Point out Plasmodium parasites and leukocytes.
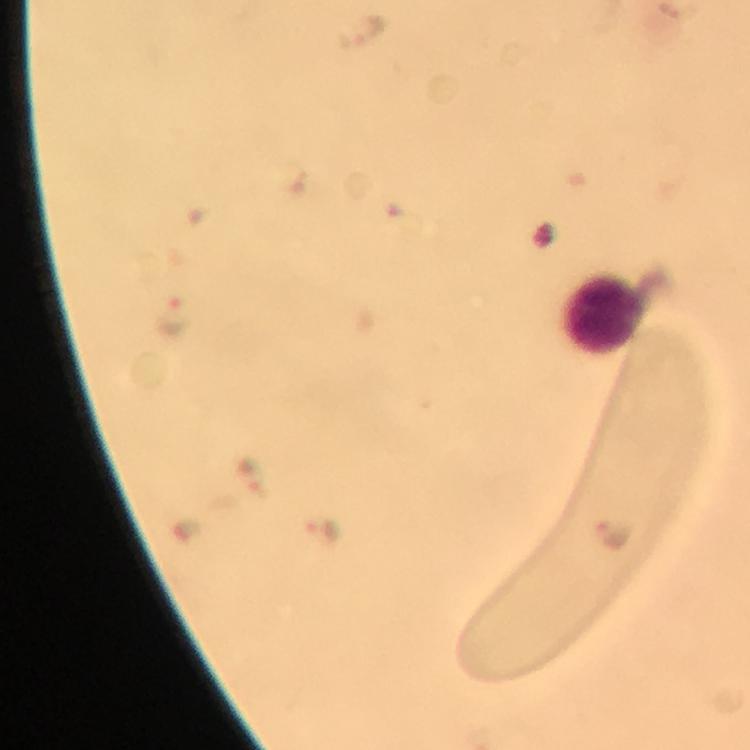

Approximate centers as (x, y) in pixels.
Plasmodium parasites: (361, 31), (173, 315), (323, 533), (615, 533).
Leukocytes: (603, 314).

At 100x magnification. Thick blood film. A crop from one field of view. Giemsa stain. Immersion oil applied. Image is 750×750 pixels. Smartphone photograph taken through a microscope. From a malaria diagnostic workup.